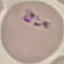

malaria status = parasitized
preparation = thin blood smear
capture = smartphone through the microscope eyepiece
stain = Giemsa
image type = automatically extracted cell patch, resized to 64 × 64 pixels